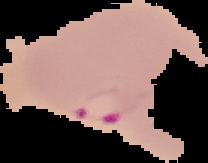

image type = segmented cell region on a black background
malaria status = parasitized
preparation = thin blood smear
image size = 208×163 pixels